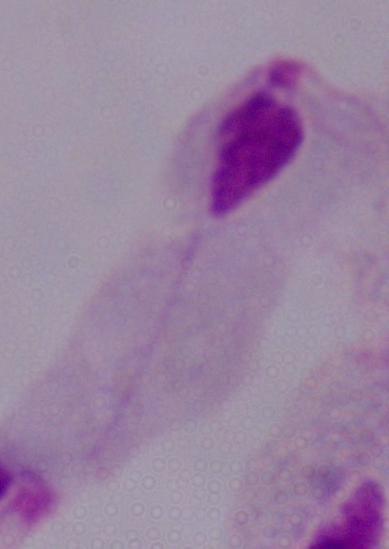

Captured at 1000x magnification. Photomicrograph. A trichomonad is seen.